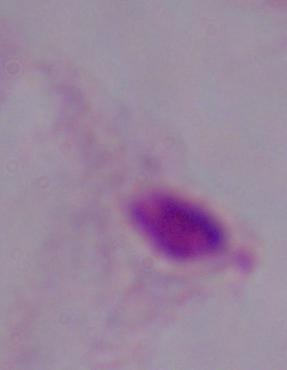
1000x magnification. Photomicrograph. A trichomonad is seen.